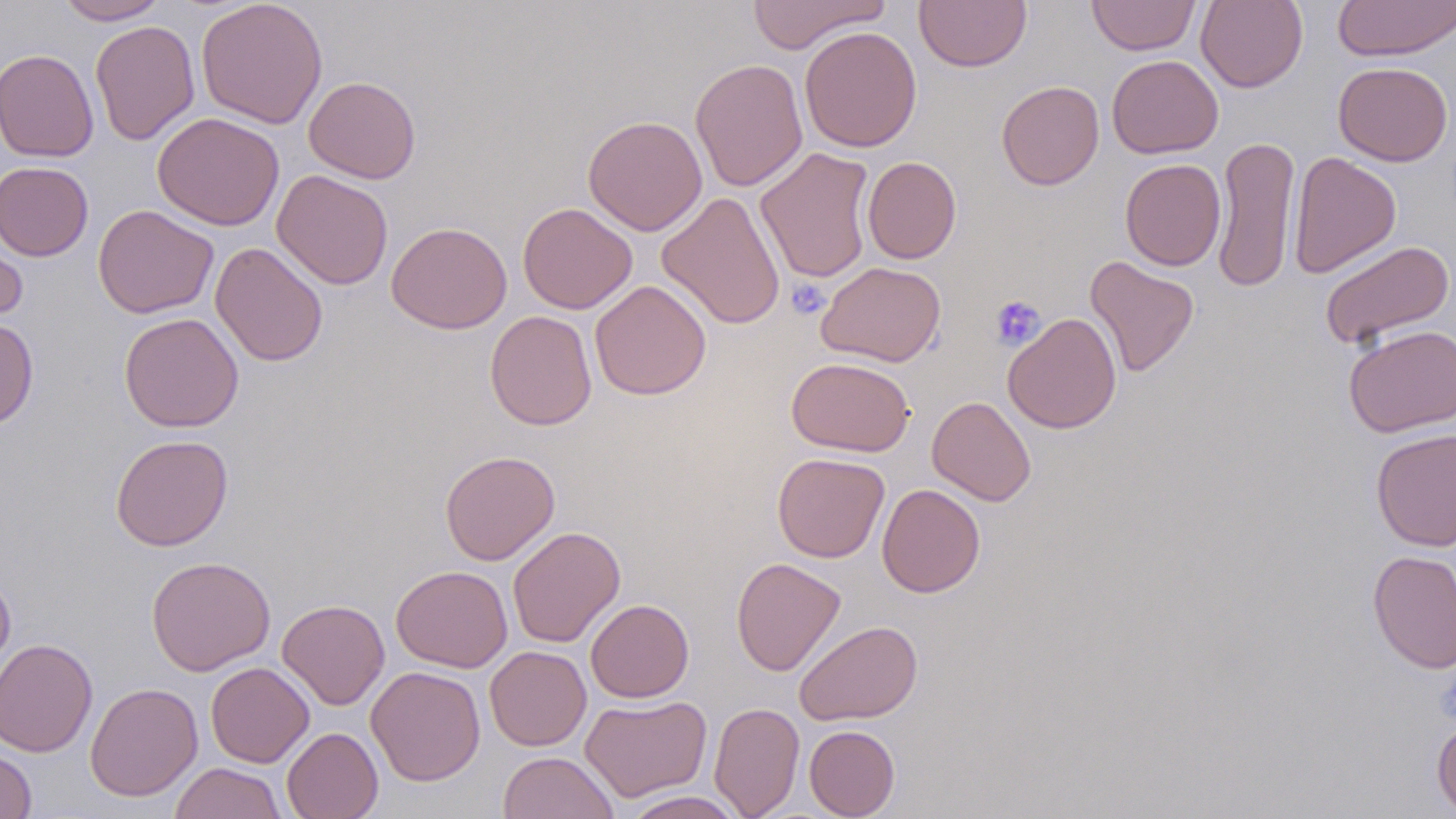

Summary:
  - Coordinate format: approximate bounding boxes as named x1/y1/x2/y2 corners in pixels
  - Uninfected red blood cell locations: (x1=56, y1=0, x2=168, y2=24), (x1=196, y1=0, x2=328, y2=129), (x1=747, y1=0, x2=890, y2=54), (x1=915, y1=0, x2=1032, y2=72), (x1=1087, y1=0, x2=1199, y2=56), (x1=1196, y1=0, x2=1308, y2=92), (x1=1333, y1=0, x2=1456, y2=62), (x1=90, y1=20, x2=200, y2=145), (x1=799, y1=26, x2=923, y2=152), (x1=0, y1=48, x2=98, y2=161), (x1=1106, y1=54, x2=1223, y2=159), (x1=690, y1=58, x2=808, y2=192), (x1=1333, y1=61, x2=1453, y2=166), (x1=304, y1=76, x2=420, y2=183), (x1=997, y1=80, x2=1104, y2=190), (x1=152, y1=112, x2=284, y2=231), (x1=582, y1=115, x2=707, y2=236), (x1=1212, y1=135, x2=1300, y2=294), (x1=755, y1=147, x2=876, y2=284), (x1=1287, y1=151, x2=1401, y2=279), (x1=862, y1=156, x2=961, y2=264), (x1=1120, y1=158, x2=1226, y2=271), (x1=0, y1=161, x2=94, y2=261), (x1=271, y1=170, x2=394, y2=289), (x1=657, y1=192, x2=786, y2=330), (x1=517, y1=202, x2=637, y2=314), (x1=93, y1=204, x2=219, y2=319), (x1=0, y1=219, x2=28, y2=328), (x1=386, y1=221, x2=512, y2=334), (x1=1319, y1=239, x2=1455, y2=350), (x1=210, y1=242, x2=328, y2=366), (x1=1084, y1=256, x2=1199, y2=377), (x1=817, y1=261, x2=946, y2=367), (x1=589, y1=280, x2=711, y2=400), (x1=485, y1=311, x2=597, y2=431), (x1=118, y1=312, x2=244, y2=432), (x1=1003, y1=312, x2=1122, y2=434), (x1=0, y1=317, x2=38, y2=430), (x1=1343, y1=324, x2=1456, y2=437), (x1=786, y1=356, x2=915, y2=457), (x1=927, y1=396, x2=1036, y2=506), (x1=1370, y1=428, x2=1456, y2=551), (x1=110, y1=434, x2=233, y2=551), (x1=440, y1=450, x2=560, y2=565), (x1=772, y1=452, x2=890, y2=563), (x1=877, y1=483, x2=985, y2=597), (x1=507, y1=526, x2=626, y2=648), (x1=1368, y1=550, x2=1456, y2=673), (x1=146, y1=556, x2=276, y2=676), (x1=730, y1=557, x2=846, y2=677), (x1=391, y1=565, x2=513, y2=672), (x1=0, y1=569, x2=16, y2=681), (x1=277, y1=599, x2=390, y2=710), (x1=585, y1=599, x2=694, y2=703), (x1=794, y1=620, x2=923, y2=725), (x1=0, y1=638, x2=99, y2=758), (x1=485, y1=645, x2=592, y2=751), (x1=206, y1=661, x2=314, y2=768), (x1=366, y1=666, x2=486, y2=786), (x1=85, y1=682, x2=203, y2=801), (x1=580, y1=694, x2=712, y2=802), (x1=709, y1=701, x2=805, y2=818), (x1=1431, y1=718, x2=1456, y2=816), (x1=804, y1=725, x2=900, y2=818), (x1=282, y1=727, x2=383, y2=819), (x1=0, y1=743, x2=37, y2=818), (x1=498, y1=751, x2=620, y2=819), (x1=169, y1=762, x2=288, y2=819), (x1=620, y1=790, x2=747, y2=819)
  - Platelet locations: (x1=787, y1=279, x2=830, y2=319), (x1=990, y1=294, x2=1047, y2=350)
  - Slide-level diagnosis: negative for blood parasites
  - Stain: May-Grünwald-Giemsa
  - Modality: optical microscopy
  - Field of view: one of a larger specimen
  - Magnification: 1000x
  - Preparation: thin blood film
  - Image size: 1456×819 pixels